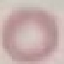 Result: no malaria parasites detected. Photographed with a smartphone camera at the microscope eyepiece. Thin smear of blood. Giemsa-stained preparation. Cell patch, automatically extracted from a larger field of view and resized to 64 × 64 pixels.